State which parasite is depicted.
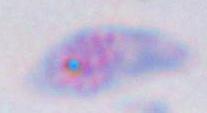

This is Toxoplasma gondii.

Summary:
  - Magnification: 1000x
  - Modality: photomicrograph